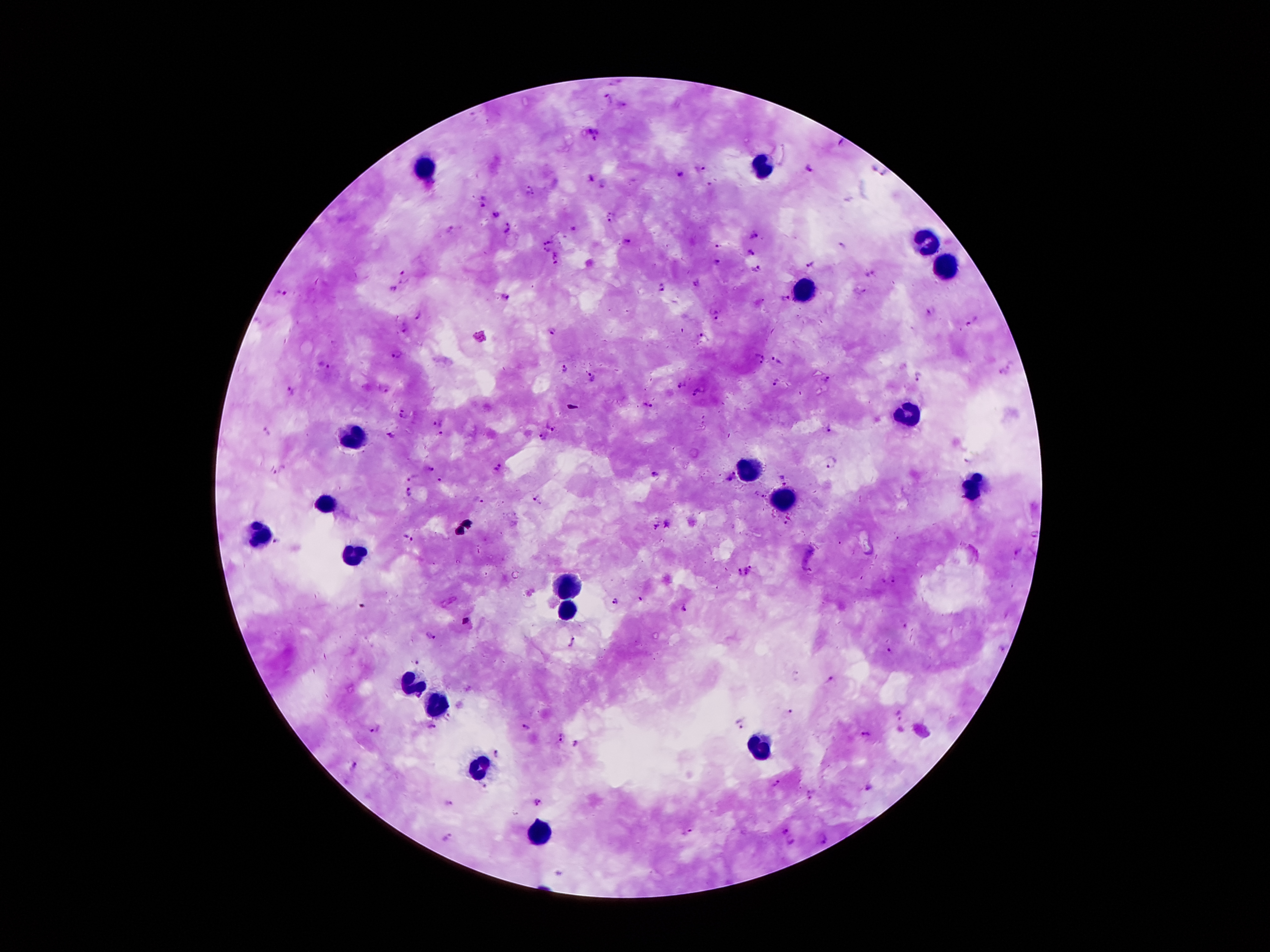
coordinate format = approximate object centers, in pixels from the top-left corner
leukocyte locations = (x=421, y=169), (x=762, y=169), (x=923, y=238), (x=942, y=263), (x=806, y=288), (x=906, y=412), (x=352, y=435), (x=749, y=471), (x=974, y=486), (x=783, y=502), (x=325, y=507), (x=260, y=536), (x=352, y=553), (x=570, y=584), (x=568, y=611), (x=407, y=687), (x=436, y=706), (x=757, y=748), (x=480, y=769), (x=539, y=834)
Plasmodium parasite locations = (x=607, y=98), (x=593, y=135), (x=700, y=168), (x=807, y=169), (x=678, y=175), (x=588, y=177), (x=602, y=182), (x=530, y=192), (x=482, y=202), (x=494, y=213), (x=608, y=217), (x=509, y=228), (x=448, y=230), (x=755, y=235), (x=549, y=240), (x=628, y=241), (x=718, y=244), (x=545, y=250), (x=750, y=253), (x=557, y=260), (x=714, y=264), (x=809, y=266), (x=755, y=268), (x=404, y=274), (x=870, y=274), (x=697, y=283), (x=662, y=286), (x=393, y=290), (x=285, y=292), (x=858, y=293), (x=505, y=297), (x=785, y=298), (x=931, y=309), (x=716, y=315), (x=418, y=316), (x=972, y=320), (x=405, y=331), (x=553, y=333), (x=706, y=338), (x=398, y=355), (x=759, y=360), (x=777, y=361), (x=323, y=366), (x=563, y=369), (x=592, y=377), (x=917, y=377), (x=827, y=379), (x=774, y=382), (x=682, y=384), (x=290, y=390), (x=698, y=393), (x=646, y=404), (x=403, y=416), (x=437, y=423), (x=553, y=424), (x=828, y=428), (x=266, y=431), (x=392, y=434), (x=441, y=435), (x=542, y=437), (x=829, y=464), (x=496, y=467), (x=430, y=468), (x=282, y=471), (x=654, y=475), (x=413, y=476), (x=732, y=476), (x=441, y=481), (x=410, y=492), (x=537, y=500), (x=479, y=501), (x=668, y=526), (x=656, y=527), (x=408, y=537), (x=278, y=541), (x=1017, y=552), (x=751, y=570), (x=738, y=574), (x=892, y=579), (x=641, y=600), (x=615, y=602), (x=685, y=608), (x=467, y=621), (x=904, y=625), (x=429, y=636), (x=574, y=640), (x=889, y=651), (x=419, y=663), (x=831, y=679), (x=790, y=711), (x=900, y=716), (x=743, y=725), (x=433, y=727), (x=528, y=727), (x=374, y=728), (x=864, y=735), (x=561, y=736), (x=577, y=743), (x=497, y=753), (x=352, y=766), (x=776, y=783), (x=484, y=786), (x=867, y=787), (x=812, y=796), (x=536, y=800), (x=448, y=802), (x=783, y=831), (x=690, y=832), (x=447, y=837), (x=820, y=839), (x=791, y=840)
magnification = 100x
patient malaria status = infected with Plasmodium falciparum
preparation = thick blood film
image size = 1270×952 pixels
stain = Giemsa
field of view = one from this slide
capture = smartphone camera through the microscope eyepiece